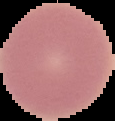
preparation: thin blood smear
image_type: cell region segmented out of the field of view; surrounding area masked to black
result: no malaria parasites seen
image_size: 115×121 pixels